Report the malaria status of this cell.
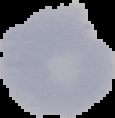
Uninfected.

image type = cell region segmented out of the field of view; surrounding area masked to black
image size = 115×118 pixels
preparation = thin blood film